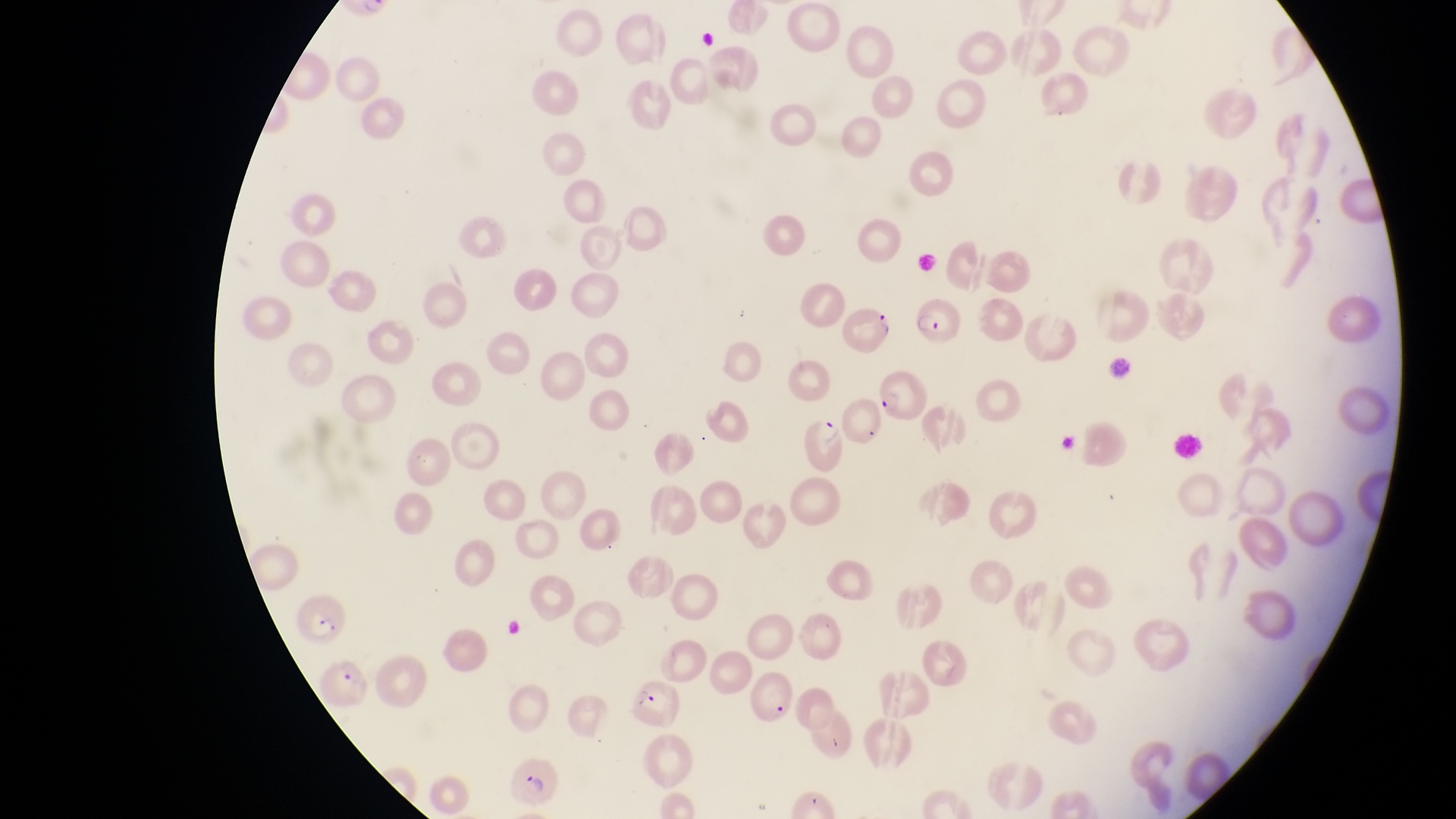
Approximate bounding boxes as {left, top, right, bottom} in pixels. Parasitised red blood cell locations: {912, 290, 967, 349}, {838, 300, 894, 360}, {874, 364, 929, 425}, {802, 416, 851, 477}, {294, 589, 353, 644}, {318, 657, 374, 712}, {632, 670, 685, 730}, {752, 670, 798, 731}, {510, 755, 566, 807}. Collected in Uganda. One field of view. Photographed through the eyepiece of an Olympus CX-23 microscope with a smartphone camera. Magnification of 1000x. Thin blood film. Image is 1456×819 pixels.